Outline each Plasmodium vivax-infected red blood cell.
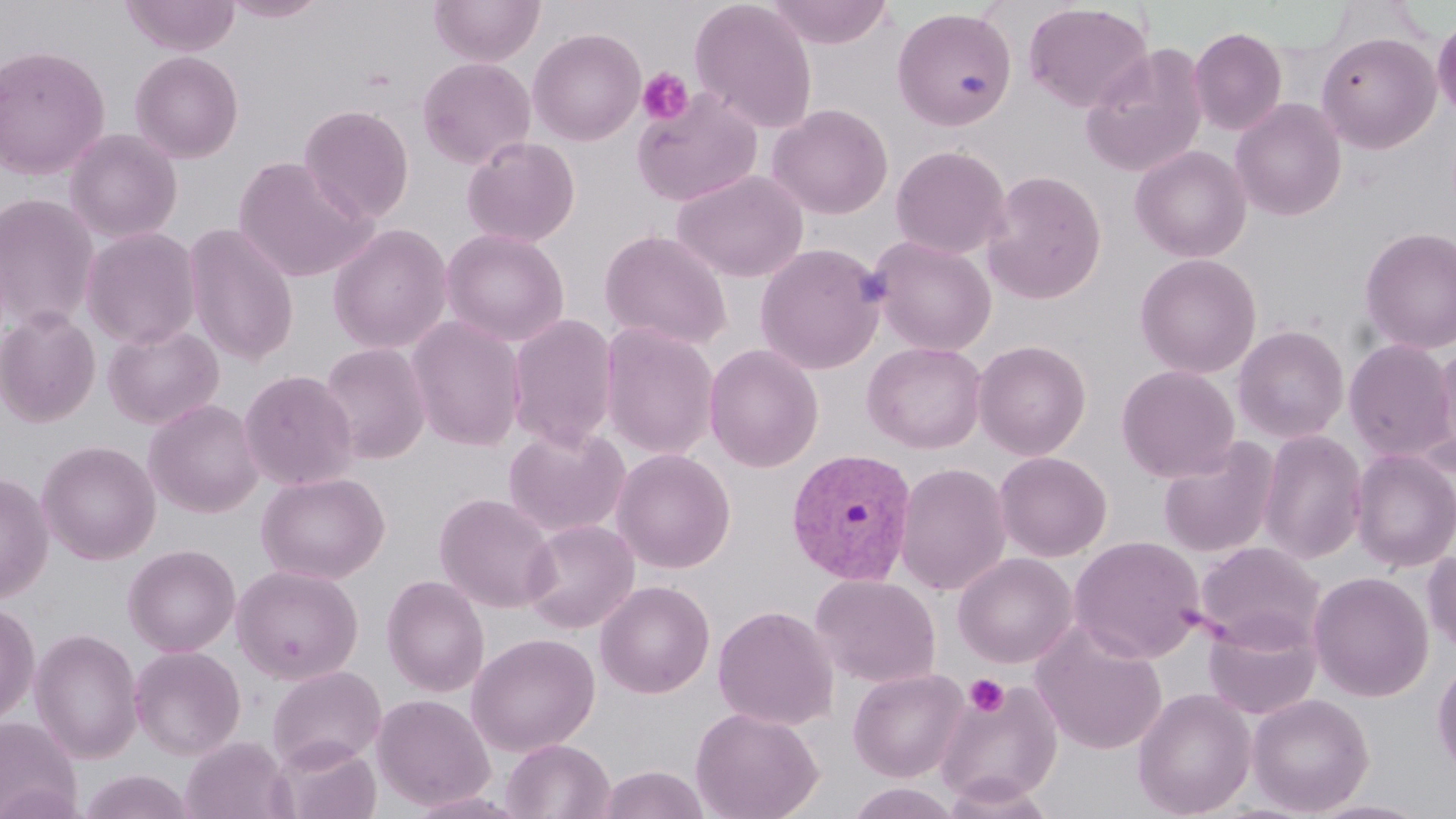
Approximate bounding boxes as [x1, y1, x2, y2] in pixels.
Plasmodium vivax-infected red blood cells: [785, 448, 918, 585].

{
  "slide_level_diagnosis": "Plasmodium vivax",
  "image_size": "1456×819 pixels",
  "preparation": "thin blood smear",
  "platelet_locations": "approximate bounding boxes as [x1, y1, x2, y2] in pixels: [637, 67, 694, 125], [965, 674, 1008, 717]",
  "uninfected_red_blood_cell_locations": "approximate bounding boxes as [x1, y1, x2, y2] in pixels: [120, 0, 241, 56], [220, 0, 331, 22], [429, 0, 545, 66], [689, 0, 818, 133], [765, 0, 894, 48], [1023, 2, 1154, 113], [892, 7, 1017, 130], [1432, 12, 1456, 122], [1188, 27, 1287, 136], [528, 28, 646, 146], [1316, 31, 1441, 154], [1080, 43, 1209, 179], [0, 45, 110, 180], [130, 51, 244, 163], [417, 57, 536, 170], [631, 87, 764, 207], [1230, 98, 1347, 221], [768, 103, 893, 219], [299, 104, 415, 222], [64, 128, 182, 243], [461, 136, 581, 248], [891, 145, 1011, 259], [1130, 145, 1252, 262], [233, 156, 376, 283], [673, 169, 808, 282], [982, 170, 1107, 304], [0, 193, 99, 331], [182, 223, 300, 366], [328, 224, 453, 355], [81, 226, 202, 349], [1359, 226, 1456, 355], [439, 228, 570, 347], [599, 229, 733, 349], [870, 236, 996, 356], [754, 242, 886, 375], [1134, 253, 1262, 378], [0, 307, 101, 427], [507, 313, 618, 451], [406, 315, 526, 452], [102, 323, 224, 429], [600, 323, 720, 460], [1232, 324, 1350, 444], [1343, 339, 1455, 462], [973, 340, 1091, 460], [862, 341, 987, 454], [318, 343, 431, 465], [703, 343, 824, 472], [1421, 344, 1456, 475], [1116, 364, 1240, 481], [239, 370, 359, 491], [144, 398, 264, 518], [503, 424, 631, 537], [1257, 429, 1368, 564], [1157, 437, 1280, 558], [38, 440, 160, 564], [611, 448, 736, 574], [1350, 448, 1456, 572], [994, 452, 1112, 561], [895, 462, 1012, 597], [1, 471, 53, 603], [256, 471, 390, 584], [435, 492, 558, 613], [520, 519, 639, 634], [1069, 535, 1206, 663], [1195, 541, 1325, 652], [123, 544, 240, 656], [1422, 548, 1456, 654], [952, 552, 1078, 668], [232, 564, 363, 684], [1308, 571, 1433, 702], [810, 573, 941, 688], [382, 575, 489, 697], [595, 580, 715, 698], [0, 601, 39, 727], [713, 604, 839, 730], [1203, 611, 1322, 720], [1031, 622, 1168, 755], [30, 628, 143, 763], [466, 632, 600, 756], [129, 644, 246, 760], [1432, 657, 1456, 776], [267, 665, 386, 771], [847, 667, 969, 782], [933, 679, 1064, 807], [1133, 687, 1256, 818], [1247, 692, 1374, 816], [372, 693, 495, 810], [691, 706, 824, 819], [0, 715, 82, 819], [180, 735, 294, 819], [501, 738, 614, 819], [271, 740, 382, 819], [598, 765, 709, 818], [78, 770, 195, 819], [1307, 799, 1435, 819]",
  "field_of_view": "one of a larger specimen",
  "magnification": "1000x",
  "stain": "May-Grünwald-Giemsa",
  "modality": "optical microscopy"
}